Report the malaria status of this cell.
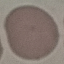

It is uninfected.

Thin smear of blood. Automatically extracted cell patch, resized to 64 × 64 pixels. Giemsa stain. Acquired by smartphone through the microscope eyepiece.